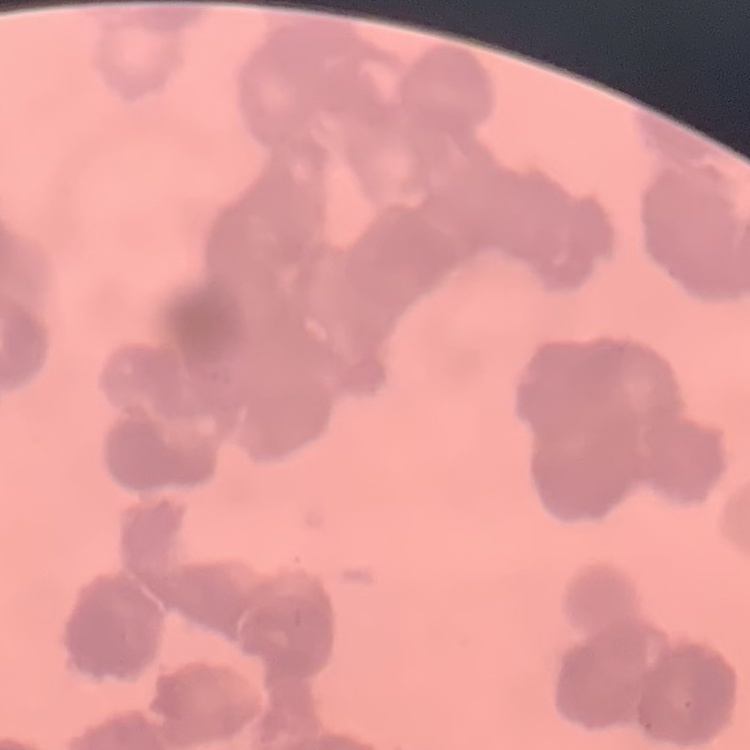

The red blood cells exhibit rouleaux formation. Thin blood film. Square crop of a larger photomicrograph. Stained with either Field's or Giemsa.